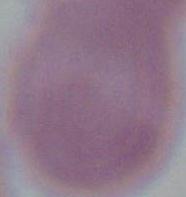

An erythrocyte is seen. Photomicrograph. 1000x magnification.